Name the parasite shown.
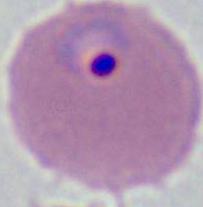

Plasmodium.

{
  "magnification": "400x or 1000x",
  "modality": "micrograph"
}